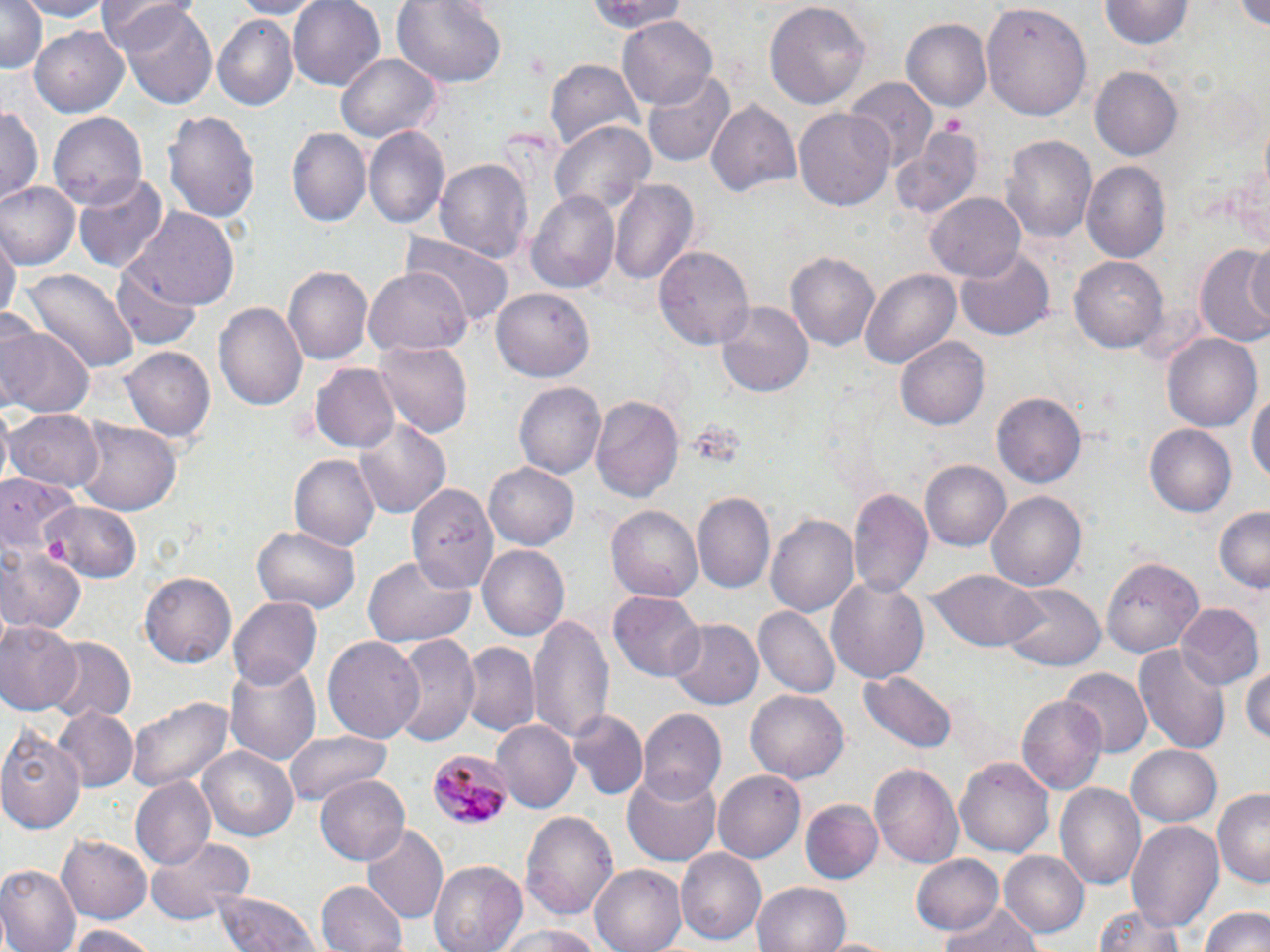
Summary:
  - Coordinate format: approximate bounding boxes as (x1,y1)-(x2,y2) corner pairs in pixels
  - Uninfected red blood cell locations: (18,0)-(112,20), (229,0)-(322,19), (288,0)-(386,92), (391,0)-(508,91), (583,0)-(689,36), (765,0)-(871,113), (0,1)-(47,75), (1100,1)-(1191,49), (101,3)-(200,58), (115,3)-(218,111), (982,5)-(1093,119), (617,15)-(718,110), (212,16)-(300,109), (900,16)-(991,110), (31,25)-(129,116), (336,52)-(442,145), (546,59)-(643,151), (1089,65)-(1183,160), (645,68)-(735,168), (843,77)-(937,171), (705,97)-(801,201), (0,103)-(42,207), (164,106)-(260,229), (795,107)-(895,212), (47,112)-(146,210), (551,121)-(657,215), (363,126)-(448,231), (892,126)-(985,219), (287,128)-(369,229), (1000,135)-(1096,244), (434,156)-(533,262), (1082,162)-(1171,263), (74,174)-(168,273), (610,178)-(698,290), (0,183)-(79,270), (527,189)-(620,293), (928,190)-(1025,279), (128,208)-(241,311), (1,228)-(17,331), (403,229)-(514,329), (1241,237)-(1268,333), (1196,244)-(1270,351), (656,246)-(754,354), (957,247)-(1054,341), (785,248)-(879,350), (1069,254)-(1168,353), (110,261)-(205,349), (283,265)-(371,366), (365,266)-(470,356), (861,267)-(963,367), (21,268)-(140,373), (492,289)-(592,381), (215,299)-(309,415), (715,300)-(814,397), (3,322)-(94,419), (1163,332)-(1262,430), (896,335)-(989,431), (373,340)-(472,439), (121,346)-(215,444), (311,362)-(401,453), (514,381)-(605,481), (1247,383)-(1270,497), (993,393)-(1086,490), (591,395)-(684,503), (7,408)-(104,491), (71,418)-(184,515), (355,418)-(451,520), (1147,424)-(1237,516), (292,453)-(381,551), (483,459)-(578,548), (919,460)-(1009,551), (0,473)-(73,559), (407,479)-(495,590), (848,488)-(932,598), (988,489)-(1087,589), (694,492)-(775,593), (41,503)-(140,583), (608,505)-(703,602), (1214,506)-(1270,593), (769,513)-(859,621), (253,523)-(358,614), (479,545)-(570,640), (0,546)-(85,635), (361,553)-(478,647), (1101,553)-(1202,655), (928,567)-(1045,653), (138,571)-(237,669), (826,574)-(929,684), (1004,582)-(1103,671), (609,592)-(705,682), (229,596)-(322,691), (1174,605)-(1262,691), (755,607)-(840,698), (529,611)-(613,747), (667,619)-(763,710), (0,620)-(80,713), (387,632)-(480,748), (323,636)-(425,744), (43,638)-(136,726), (460,643)-(539,738), (1133,643)-(1231,754), (226,663)-(319,765), (1243,664)-(1270,747), (1061,667)-(1151,756), (860,671)-(957,753), (746,689)-(848,784), (1018,695)-(1107,794), (127,697)-(233,795), (54,706)-(138,789), (636,708)-(724,804), (570,711)-(648,801), (490,721)-(578,814), (1,723)-(85,834), (286,728)-(394,805), (1126,743)-(1224,827), (197,745)-(298,839), (956,755)-(1054,860), (869,763)-(965,869), (622,765)-(725,866), (712,769)-(805,864), (315,774)-(412,865), (131,778)-(216,869), (1056,782)-(1147,892), (1212,788)-(1269,885), (800,800)-(882,883), (519,810)-(620,923), (1126,820)-(1224,929), (360,824)-(449,924), (57,832)-(152,923), (146,835)-(252,926), (675,848)-(766,946), (998,850)-(1089,939), (912,854)-(1004,934), (428,859)-(527,952), (589,864)-(687,952), (0,866)-(79,952), (316,880)-(406,952), (753,881)-(852,952), (212,889)-(322,952), (1093,900)-(1194,952), (935,903)-(1046,952), (1202,905)-(1269,952), (67,925)-(163,952), (493,926)-(613,951), (822,934)-(896,952)
  - Plasmodium malariae-infected red blood cell locations: (426,748)-(512,829)
  - Slide-level diagnosis: Plasmodium malariae
  - Image size: 1270×952 pixels
  - Magnification: 1000x
  - Preparation: thin blood smear
  - Modality: light microscopy
  - Field of view: one of a larger specimen
  - Stain: May-Grünwald-Giemsa